Assess the morphology of the erythrocytes.
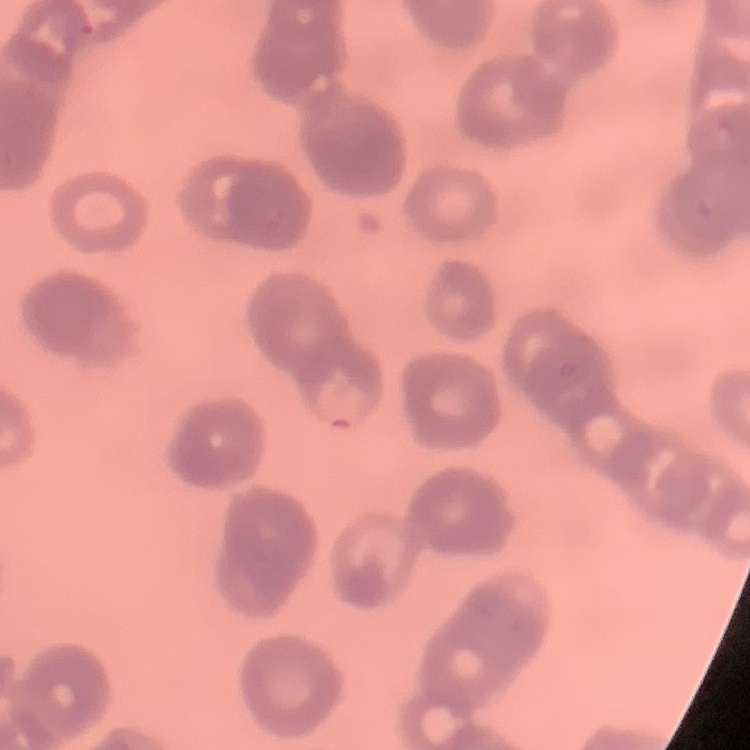

They show rouleaux formation.

Summary:
  - Image type: one tile cut from a larger photomicrograph
  - Preparation: thin blood smear
  - Stain: Field's or Giemsa